Identify the blood parasite species.
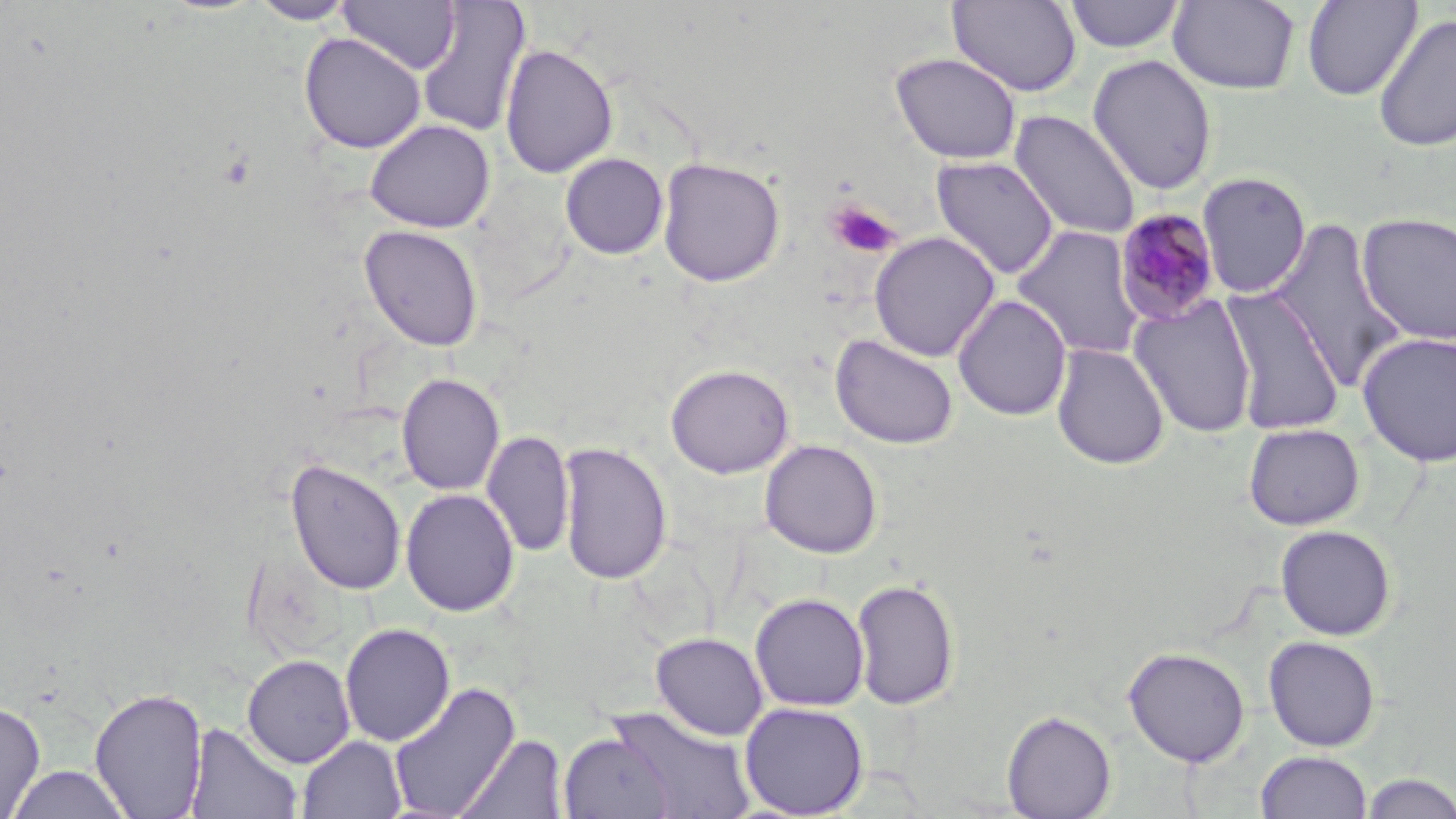

Plasmodium malariae.

Approximate bounding boxes as [x1, y1, x2, y2] in pixels. Uninfected red blood cell locations: [1063, 0, 1185, 53], [1301, 0, 1421, 101], [250, 1, 357, 25], [338, 1, 461, 75], [416, 1, 531, 138], [947, 1, 1082, 97], [1167, 1, 1301, 94], [1373, 13, 1456, 153], [299, 32, 427, 154], [500, 43, 618, 179], [890, 52, 1022, 165], [1088, 54, 1217, 195], [1009, 110, 1141, 240], [364, 118, 496, 233], [560, 153, 669, 259], [931, 156, 1060, 280], [657, 157, 785, 287], [1197, 171, 1311, 298], [1356, 212, 1456, 345], [1266, 218, 1409, 392], [358, 224, 484, 352], [1011, 225, 1148, 361], [869, 231, 1000, 362], [1220, 286, 1345, 434], [953, 294, 1072, 421], [1129, 295, 1259, 438], [1356, 331, 1456, 468], [830, 333, 958, 449], [1051, 343, 1170, 470], [665, 363, 794, 478], [396, 373, 505, 495], [1243, 423, 1364, 530], [482, 429, 575, 559], [556, 439, 672, 586], [759, 439, 883, 558], [285, 457, 407, 596], [287, 475, 521, 605], [400, 488, 520, 617], [1275, 524, 1397, 640], [850, 577, 961, 711], [750, 592, 870, 712], [339, 623, 456, 747], [650, 631, 768, 741], [1262, 635, 1381, 751], [1123, 646, 1250, 766], [242, 654, 356, 768], [387, 682, 522, 818], [89, 686, 209, 819], [0, 700, 46, 819], [738, 701, 869, 818], [601, 706, 756, 819], [1001, 710, 1116, 818], [185, 722, 302, 819], [558, 731, 676, 818], [454, 733, 570, 819], [296, 735, 407, 818], [1255, 750, 1373, 818], [6, 764, 133, 818], [1360, 772, 1456, 818]. Plasmodium malariae-infected red blood cell locations: [1114, 208, 1223, 326]. Platelet locations: [825, 198, 900, 258]. Image is 1456×819 pixels. Light microscopy. Thin blood smear. 1000x magnification. Single field of view. May-Grünwald-Giemsa stain.